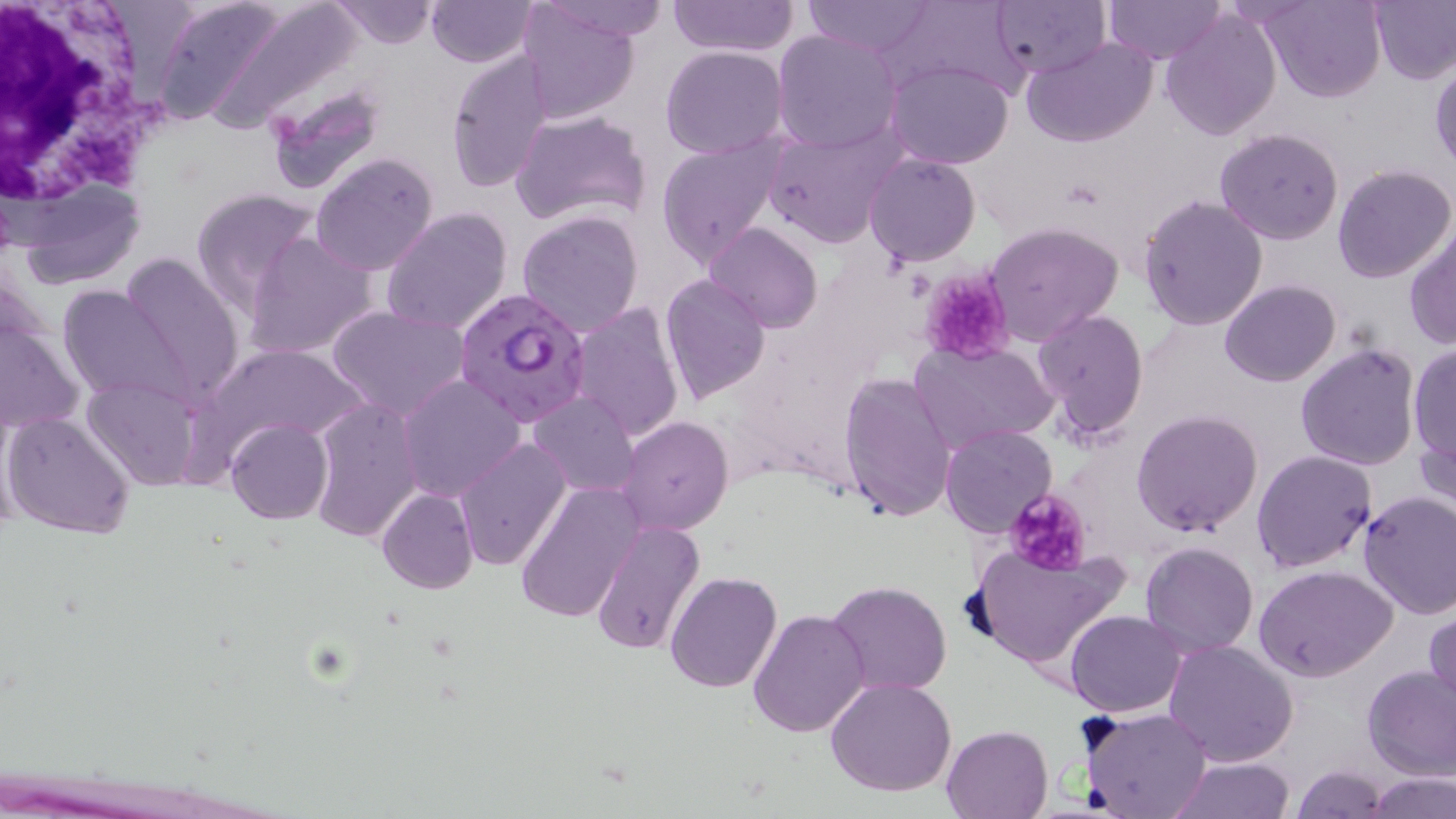

{
  "slide_level_diagnosis": "Plasmodium falciparum",
  "magnification": "1000x",
  "field_of_view": "one of a larger specimen",
  "white_blood_cell_locations": "approximate bounding boxes as [x1, y1, x2, y2] in pixels: [1, 0, 170, 216]",
  "preparation": "thin blood smear",
  "image_size": "1456×819 pixels",
  "uninfected_red_blood_cell_locations": "approximate bounding boxes as [x1, y1, x2, y2] in pixels: [149, 0, 298, 127], [202, 0, 368, 131], [327, 0, 438, 48], [534, 0, 671, 42], [670, 0, 798, 57], [803, 0, 935, 57], [894, 0, 1026, 99], [1105, 0, 1222, 63], [1261, 0, 1383, 103], [1369, 0, 1456, 85], [425, 1, 536, 68], [991, 1, 1109, 80], [515, 2, 639, 124], [1161, 8, 1282, 140], [772, 28, 902, 153], [1022, 37, 1158, 149], [660, 46, 788, 160], [446, 49, 557, 193], [885, 60, 1015, 169], [1430, 63, 1455, 171], [265, 82, 385, 196], [509, 109, 653, 228], [763, 121, 904, 248], [1214, 128, 1344, 245], [658, 135, 785, 267], [310, 152, 439, 276], [863, 153, 980, 267], [1332, 164, 1456, 283], [13, 179, 147, 293], [190, 187, 321, 315], [1138, 196, 1267, 331], [382, 206, 513, 337], [516, 210, 644, 338], [982, 221, 1123, 345], [703, 222, 823, 333], [1405, 228, 1456, 348], [244, 232, 381, 360], [118, 252, 246, 404], [660, 274, 770, 404], [1220, 279, 1340, 386], [57, 284, 193, 407], [568, 301, 686, 445], [327, 306, 471, 422], [1032, 307, 1149, 439], [0, 310, 84, 440], [910, 339, 1058, 452], [1294, 342, 1421, 469], [1408, 343, 1456, 467], [841, 373, 956, 524], [81, 374, 205, 491], [398, 375, 525, 501], [528, 392, 641, 498], [309, 395, 425, 545], [1131, 409, 1262, 538], [2, 410, 138, 540], [1416, 411, 1456, 522], [615, 417, 735, 536], [226, 418, 332, 524], [942, 426, 1056, 536], [453, 438, 572, 571], [1252, 448, 1379, 573], [516, 481, 639, 623], [378, 489, 477, 595], [1357, 492, 1456, 620], [592, 520, 704, 654], [1140, 541, 1258, 657], [965, 543, 1128, 674], [1256, 567, 1396, 683], [665, 572, 781, 694], [826, 579, 952, 699], [747, 608, 870, 737], [1426, 608, 1456, 716], [1066, 611, 1187, 716], [1163, 640, 1298, 768], [1362, 666, 1456, 781], [826, 676, 956, 797], [1081, 708, 1211, 819], [941, 724, 1054, 818], [1167, 758, 1296, 817], [1293, 764, 1388, 819], [1366, 771, 1454, 819]",
  "platelet_locations": "approximate bounding boxes as [x1, y1, x2, y2] in pixels: [919, 269, 1015, 363], [1003, 488, 1093, 573]",
  "modality": "optical microscopy",
  "plasmodium_falciparum_infected_red_blood_cell_locations": "approximate bounding boxes as [x1, y1, x2, y2] in pixels: [455, 288, 591, 425]",
  "stain": "May-Grünwald-Giemsa"
}